Name the parasite shown.
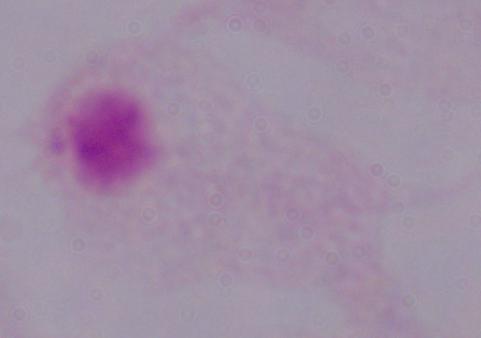
A trichomonad.

Summary:
  - Modality: micrograph
  - Magnification: 1000x